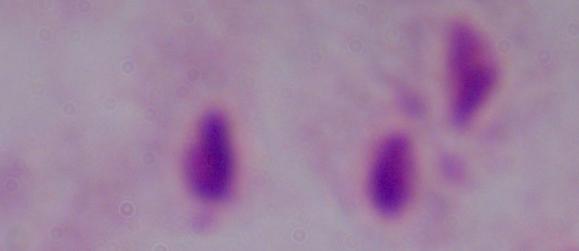
Summary:
  - Identification: trichomonad
  - Modality: micrograph
  - Magnification: 1000x